Outline each Plasmodium falciparum-infected red blood cell.
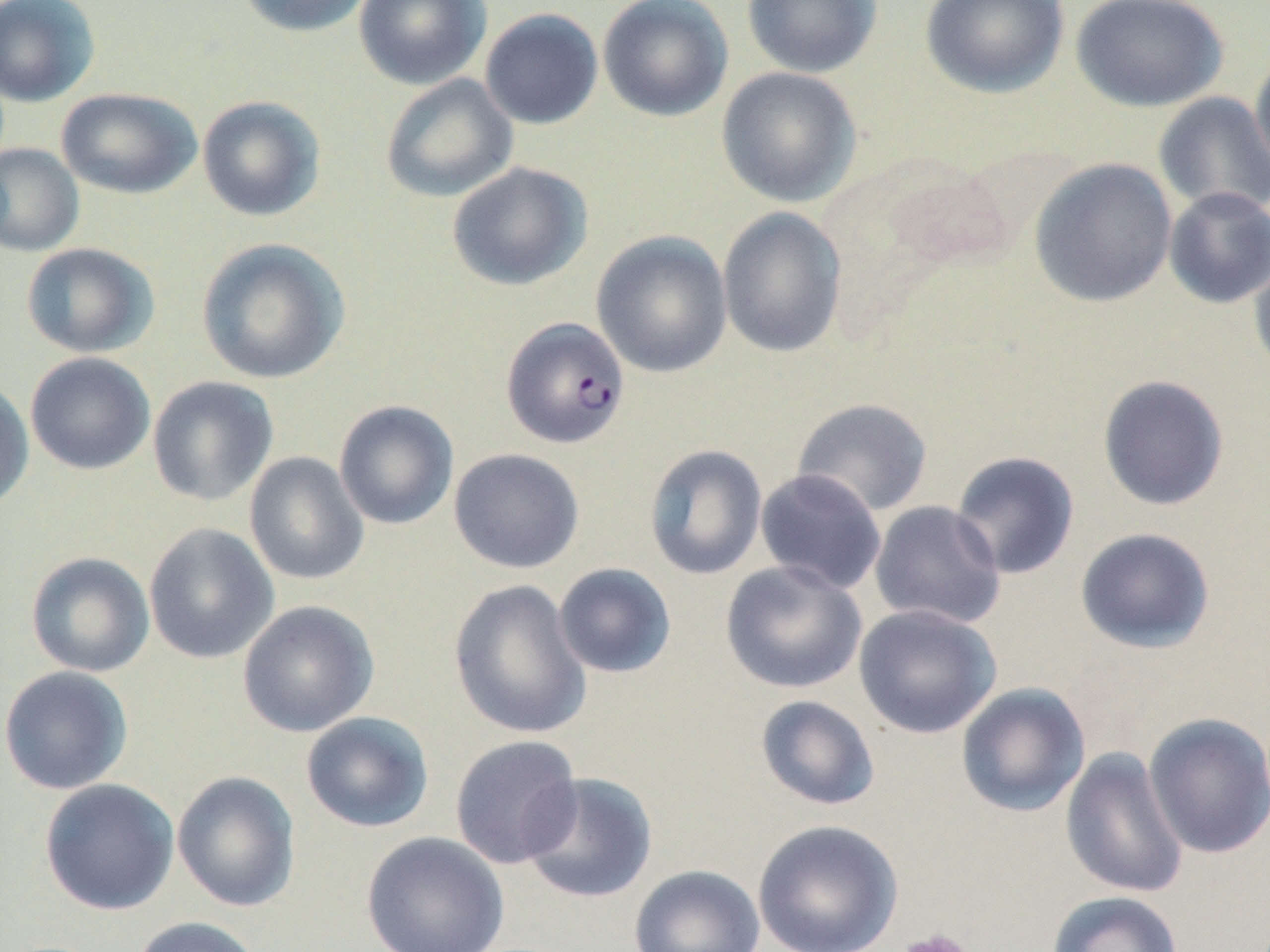

Approximate bounding boxes as (x1, y1, x2, y2) in pixels.
Plasmodium falciparum-infected red blood cells: (500, 316, 630, 449).

Uninfected red blood cell locations: (0, 0, 101, 106), (234, 0, 374, 38), (353, 0, 491, 89), (597, 0, 734, 122), (742, 0, 884, 78), (920, 0, 1070, 99), (1069, 0, 1229, 112), (479, 8, 604, 130), (1249, 49, 1270, 187), (716, 66, 862, 208), (380, 74, 518, 203), (56, 87, 202, 199), (1153, 92, 1270, 218), (197, 95, 326, 222), (0, 143, 84, 257), (1029, 158, 1178, 308), (446, 161, 592, 291), (1163, 187, 1270, 309), (717, 207, 848, 358), (591, 231, 733, 378), (195, 238, 351, 385), (21, 242, 159, 358), (1248, 253, 1270, 381), (25, 352, 156, 475), (1097, 374, 1230, 511), (147, 376, 279, 506), (0, 379, 34, 514), (791, 397, 934, 517), (334, 400, 459, 530), (644, 444, 768, 580), (448, 448, 584, 574), (950, 450, 1081, 580), (244, 452, 369, 586), (755, 469, 887, 595), (869, 501, 1007, 629), (143, 523, 280, 664), (1075, 527, 1216, 654), (25, 552, 155, 677), (720, 560, 867, 694), (553, 563, 677, 679), (447, 578, 591, 739), (237, 600, 379, 737), (853, 604, 1001, 738), (0, 666, 134, 795), (955, 682, 1090, 817), (755, 695, 880, 811), (300, 711, 434, 833), (1143, 711, 1270, 860), (449, 734, 583, 870), (1060, 746, 1188, 899), (172, 770, 301, 913), (518, 772, 658, 904), (38, 778, 180, 915), (752, 819, 904, 952), (361, 831, 509, 952), (629, 864, 765, 952), (1045, 890, 1184, 952), (130, 916, 263, 952). Platelet locations: (896, 929, 977, 952). Slide-level diagnosis: Plasmodium falciparum. 1000x magnification. Thin blood film. May-Grünwald-Giemsa stain. One field of a larger specimen. Image is 1270×952 pixels. Optical microscopy.